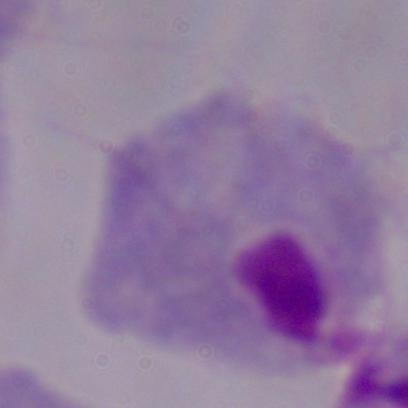
Summary:
  - Modality: micrograph
  - Magnification: 1000x
  - Identification: trichomonad